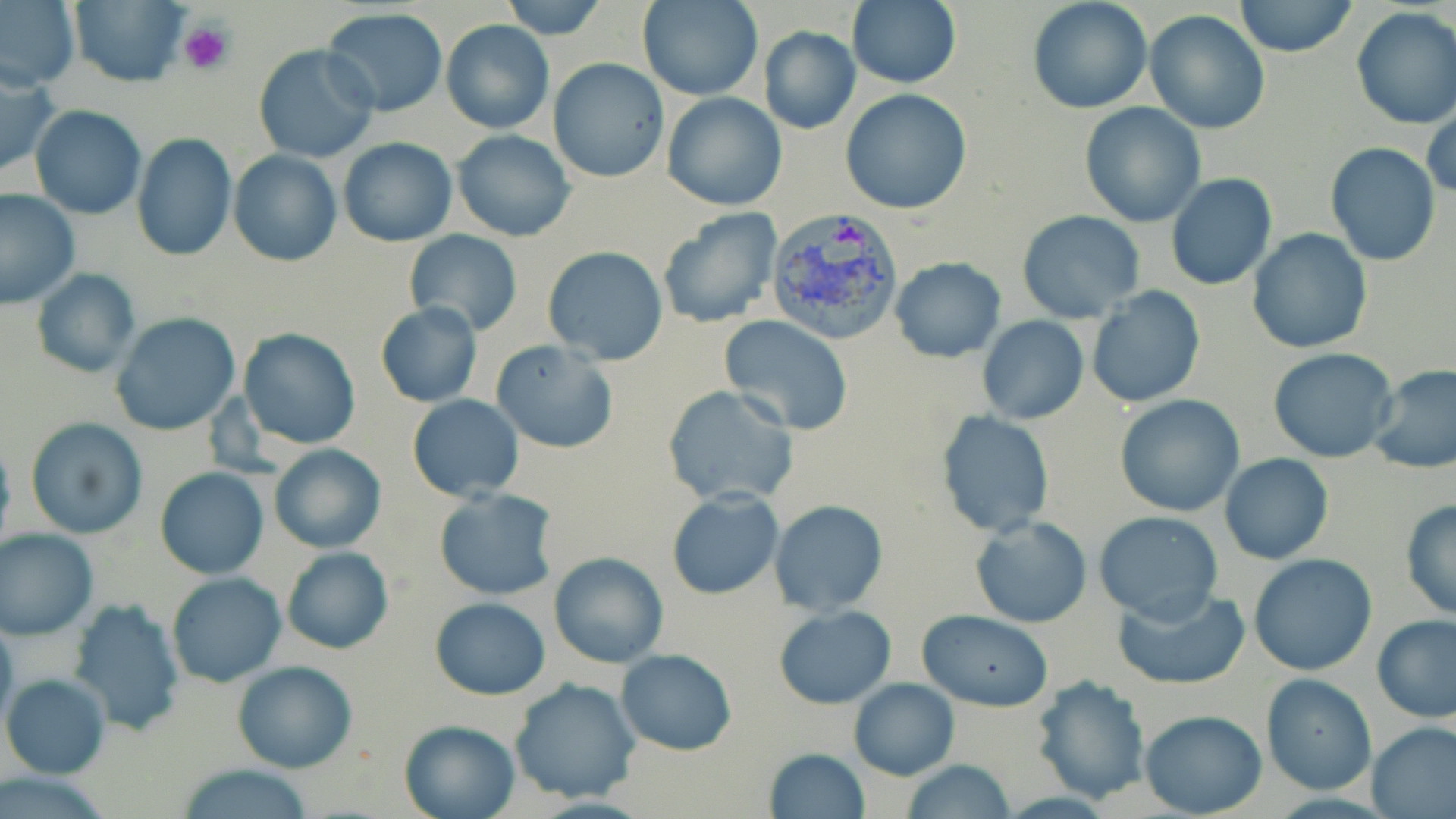

Summary:
  - Coordinate format: approximate bounding boxes as named x1/y1/x2/y2 corners in pixels
  - Platelet locations: (x1=180, y1=19, x2=234, y2=75)
  - Uninfected red blood cell locations: (x1=0, y1=0, x2=81, y2=91), (x1=68, y1=0, x2=190, y2=87), (x1=499, y1=0, x2=609, y2=40), (x1=847, y1=0, x2=961, y2=88), (x1=1233, y1=0, x2=1358, y2=57), (x1=637, y1=1, x2=764, y2=102), (x1=1026, y1=1, x2=1153, y2=115), (x1=1350, y1=6, x2=1456, y2=129), (x1=323, y1=7, x2=448, y2=116), (x1=1145, y1=9, x2=1271, y2=134), (x1=441, y1=19, x2=554, y2=133), (x1=757, y1=27, x2=860, y2=134), (x1=253, y1=44, x2=381, y2=165), (x1=548, y1=57, x2=669, y2=183), (x1=0, y1=61, x2=58, y2=180), (x1=840, y1=89, x2=972, y2=213), (x1=661, y1=91, x2=785, y2=209), (x1=1425, y1=101, x2=1456, y2=202), (x1=1080, y1=102, x2=1205, y2=227), (x1=29, y1=105, x2=146, y2=219), (x1=452, y1=128, x2=576, y2=241), (x1=131, y1=133, x2=237, y2=261), (x1=337, y1=138, x2=457, y2=247), (x1=1324, y1=143, x2=1440, y2=267), (x1=228, y1=150, x2=342, y2=266), (x1=1166, y1=173, x2=1277, y2=290), (x1=1, y1=189, x2=79, y2=308), (x1=655, y1=209, x2=782, y2=330), (x1=1016, y1=210, x2=1146, y2=323), (x1=1246, y1=229, x2=1373, y2=354), (x1=404, y1=231, x2=523, y2=338), (x1=1045, y1=242, x2=1180, y2=386), (x1=541, y1=247, x2=669, y2=365), (x1=891, y1=257, x2=1006, y2=361), (x1=32, y1=269, x2=142, y2=378), (x1=1085, y1=285, x2=1205, y2=407), (x1=373, y1=303, x2=482, y2=408), (x1=111, y1=312, x2=242, y2=436), (x1=719, y1=315, x2=854, y2=434), (x1=976, y1=316, x2=1089, y2=424), (x1=238, y1=329, x2=361, y2=448), (x1=490, y1=340, x2=618, y2=454), (x1=1267, y1=348, x2=1398, y2=463), (x1=1367, y1=362, x2=1456, y2=474), (x1=663, y1=385, x2=797, y2=505), (x1=1116, y1=393, x2=1245, y2=517), (x1=408, y1=394, x2=524, y2=502), (x1=936, y1=411, x2=1054, y2=536), (x1=25, y1=419, x2=148, y2=538), (x1=268, y1=443, x2=386, y2=553), (x1=1220, y1=454, x2=1333, y2=565), (x1=155, y1=467, x2=268, y2=579), (x1=433, y1=489, x2=559, y2=600), (x1=666, y1=489, x2=783, y2=599), (x1=770, y1=500, x2=888, y2=614), (x1=1399, y1=500, x2=1456, y2=621), (x1=1093, y1=510, x2=1224, y2=624), (x1=970, y1=515, x2=1092, y2=626), (x1=0, y1=529, x2=98, y2=640), (x1=280, y1=546, x2=393, y2=654), (x1=549, y1=552, x2=669, y2=667), (x1=1249, y1=554, x2=1379, y2=676), (x1=166, y1=573, x2=287, y2=688), (x1=1112, y1=584, x2=1251, y2=691), (x1=431, y1=597, x2=550, y2=700), (x1=68, y1=598, x2=186, y2=735), (x1=772, y1=605, x2=895, y2=709), (x1=917, y1=609, x2=1054, y2=710), (x1=1373, y1=616, x2=1456, y2=723), (x1=617, y1=648, x2=736, y2=754), (x1=231, y1=660, x2=357, y2=773), (x1=2, y1=673, x2=110, y2=778), (x1=1030, y1=675, x2=1150, y2=803), (x1=1261, y1=675, x2=1377, y2=793), (x1=848, y1=677, x2=958, y2=780), (x1=509, y1=678, x2=640, y2=803), (x1=1139, y1=709, x2=1267, y2=817), (x1=398, y1=719, x2=520, y2=819), (x1=1366, y1=720, x2=1456, y2=819), (x1=762, y1=748, x2=870, y2=819), (x1=902, y1=760, x2=1018, y2=818), (x1=175, y1=763, x2=317, y2=818)
  - Plasmodium vivax-infected red blood cell locations: (x1=765, y1=209, x2=908, y2=345)
  - Slide-level diagnosis: Plasmodium vivax
  - Preparation: thin blood film
  - Stain: May-Grünwald-Giemsa
  - Image size: 1456×819 pixels
  - Modality: optical microscopy
  - Magnification: 1000x
  - Field of view: single